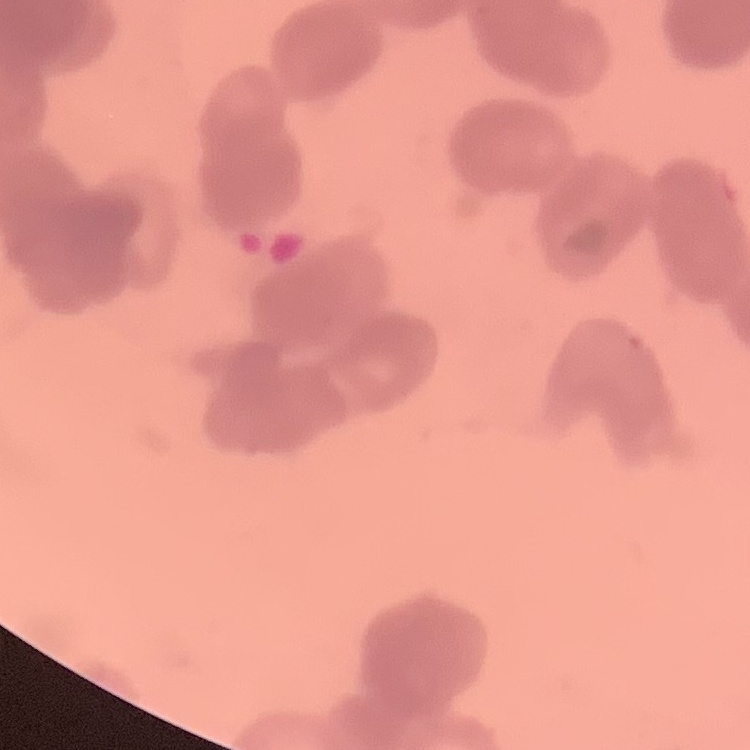

Summary:
  - Red blood cell morphology: rouleaux formation
  - Stain: Field's or Giemsa
  - Image type: square crop of a larger photomicrograph
  - Preparation: thin peripheral smear